Assess this cell for malaria.
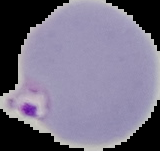

It is parasitized.

image type = segmented cell region on a black background
image size = 160×151 pixels
preparation = thin blood film